Assess this cell for malaria.
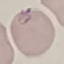

Parasitized.

Acquired by smartphone through the microscope eyepiece. Automatically extracted cell patch, resized to 64 × 64 pixels. Giemsa-stained preparation. Thin blood film.